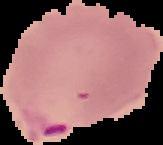

result = malaria parasites identified
image size = 163×145 pixels
image type = segmented cell region on a black background
preparation = thin blood smear